Assess this cell for malaria.
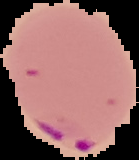

Parasitized.

Summary:
  - Preparation: thin blood smear
  - Image type: segmented cell region with the area outside set to black
  - Image size: 139×160 pixels